State which parasite is depicted.
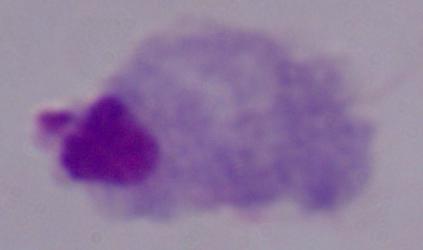
A trichomonad.

modality = micrograph
magnification = 1000x